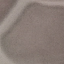
Result: no malaria parasites detected. Acquired by smartphone through the microscope eyepiece. Thin blood film. Cell patch, automatically extracted from a larger field of view and resized to 64 × 64 pixels. Giemsa stain.